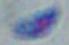
modality = micrograph
identification = Toxoplasma gondii
magnification = 1000x